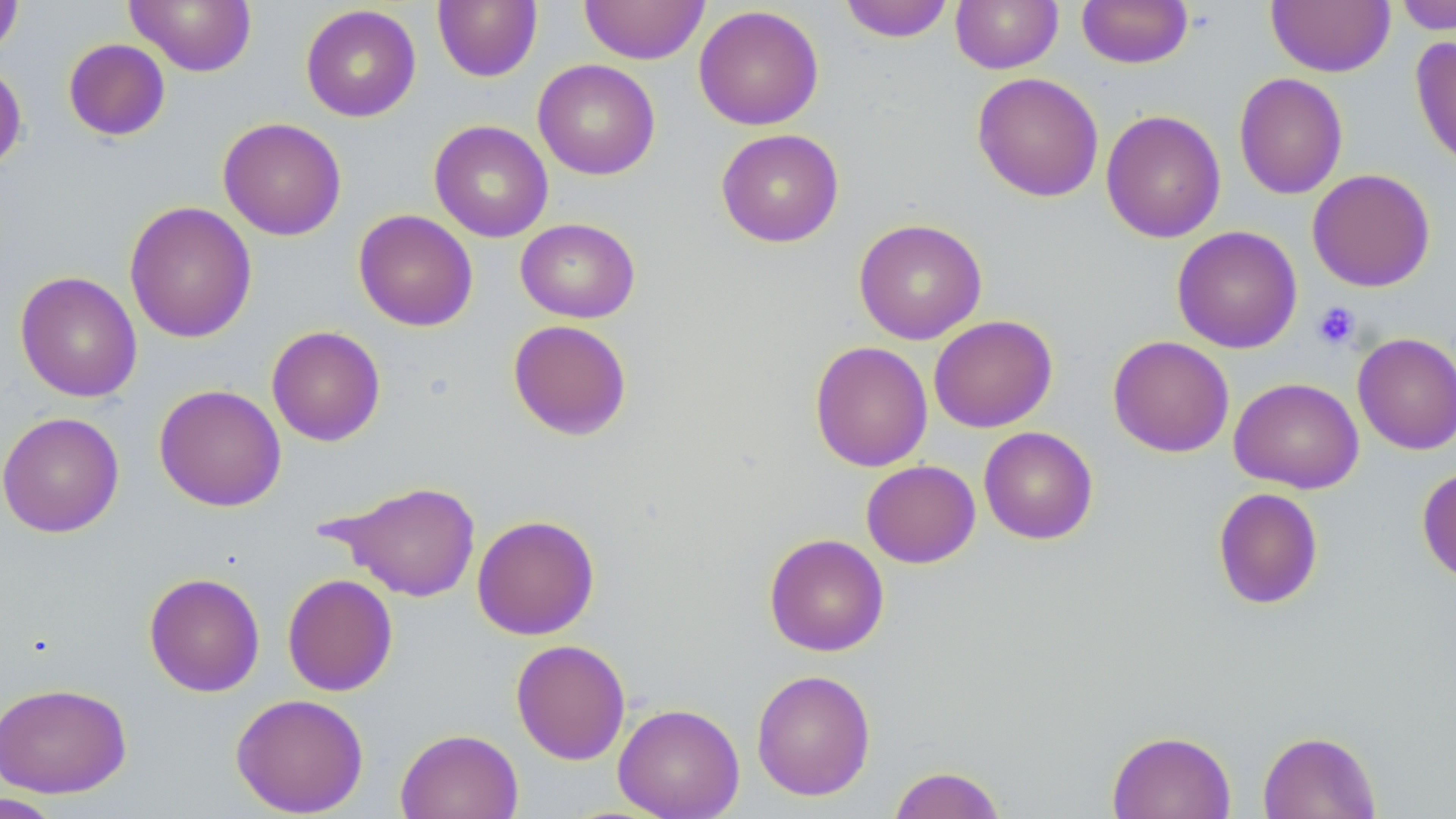
slide_level_diagnosis: negative for blood parasites
platelet_locations: 'approximate bounding boxes as (x1, y1, x2, y2) in pixels: (1312, 300, 1361, 350)'
stain: May-Grünwald-Giemsa
uninfected_red_blood_cell_locations: 'approximate bounding boxes as (x1, y1, x2, y2) in pixels: (0, 0, 24, 59), (124, 0, 257, 76), (432, 0, 542, 83), (579, 0, 709, 65), (838, 0, 955, 43), (950, 0, 1063, 74), (1077, 0, 1193, 68), (1266, 1, 1395, 77), (1393, 1, 1456, 35), (300, 4, 421, 122), (693, 5, 824, 131), (1410, 35, 1456, 173), (63, 38, 171, 142), (0, 59, 27, 175), (532, 59, 661, 180), (972, 72, 1104, 203), (1233, 72, 1348, 200), (1100, 110, 1226, 243), (217, 117, 347, 241), (429, 120, 553, 243), (715, 128, 844, 247), (1307, 168, 1436, 292), (124, 201, 257, 343), (353, 209, 478, 331), (515, 218, 640, 323), (853, 218, 987, 344), (1171, 226, 1303, 353), (15, 271, 142, 402), (928, 315, 1057, 433), (507, 319, 633, 441), (266, 325, 386, 446), (1352, 332, 1456, 455), (1107, 335, 1235, 457), (809, 340, 933, 472), (1228, 376, 1364, 494), (154, 384, 286, 512), (0, 411, 124, 538), (978, 426, 1098, 545), (861, 460, 981, 568), (1416, 465, 1456, 585), (328, 480, 482, 602), (1212, 487, 1324, 610), (471, 514, 600, 640), (764, 533, 889, 657), (143, 572, 265, 697), (282, 573, 398, 697), (510, 639, 631, 765), (751, 669, 876, 801), (0, 682, 132, 798), (230, 693, 369, 817), (613, 702, 745, 818), (395, 728, 523, 819), (1107, 730, 1236, 819), (1257, 730, 1381, 818), (887, 765, 1007, 818), (0, 792, 67, 818)'
magnification: 1000x
field_of_view: one of a larger specimen
modality: light microscopy
preparation: thin blood smear
image_size: 1456×819 pixels